Name the parasite shown.
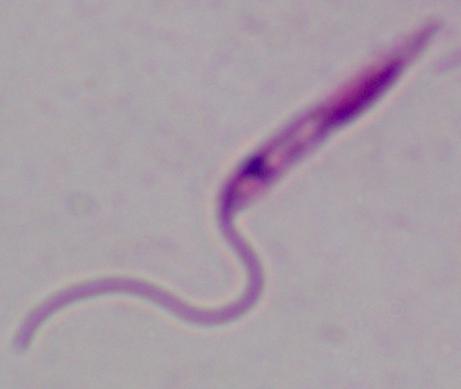

Leishmania.

Micrograph. Captured at 1000x magnification.